Identify the parasite.
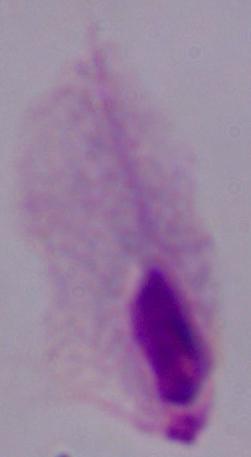
This is a trichomonad.

Summary:
  - Magnification: 1000x
  - Modality: micrograph